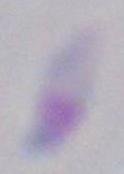

Summary:
  - Magnification: 1000x
  - Modality: micrograph
  - Identification: Toxoplasma gondii